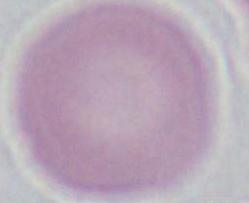 A red blood cell is shown. Captured at 1000x magnification. Micrograph.